Name the parasite shown.
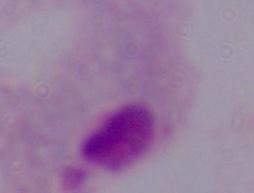
A trichomonad.

magnification = 1000x
modality = photomicrograph